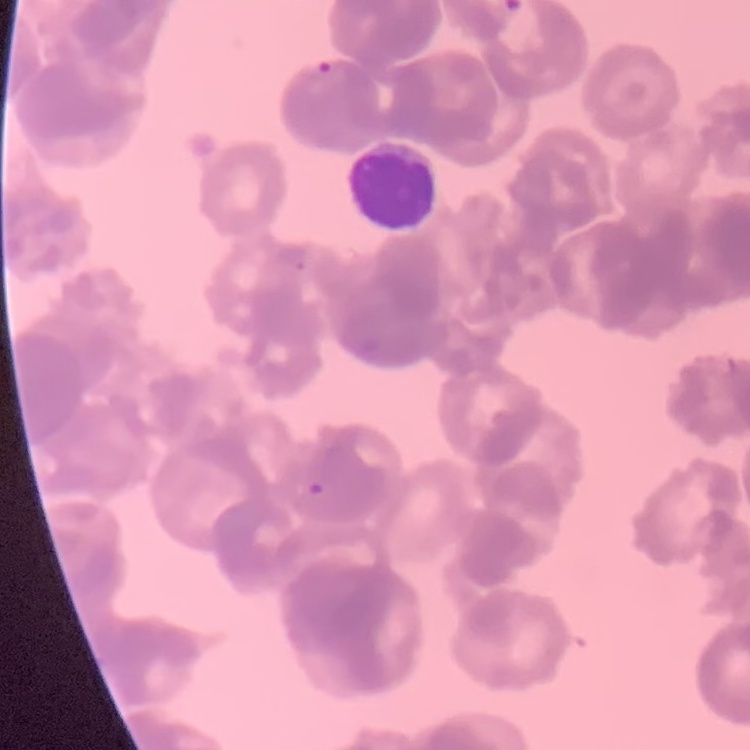
The erythrocytes show rouleaux formation. Thin peripheral smear. One tile cut from a larger photomicrograph. Stained with either Field's or Giemsa.